State which parasite is depicted.
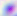

Toxoplasma gondii.

Summary:
  - Magnification: 400x
  - Modality: photomicrograph